Classify this cell by malaria status.
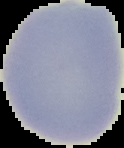

Uninfected.

Image is 124×148 pixels. Segmented cell region on a black background. From a thin blood smear.